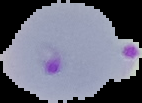

{
  "image_size": "142×103 pixels",
  "image_type": "segmented cell region with the area outside set to black",
  "result": "Plasmodium parasites detected",
  "preparation": "thin blood smear"
}